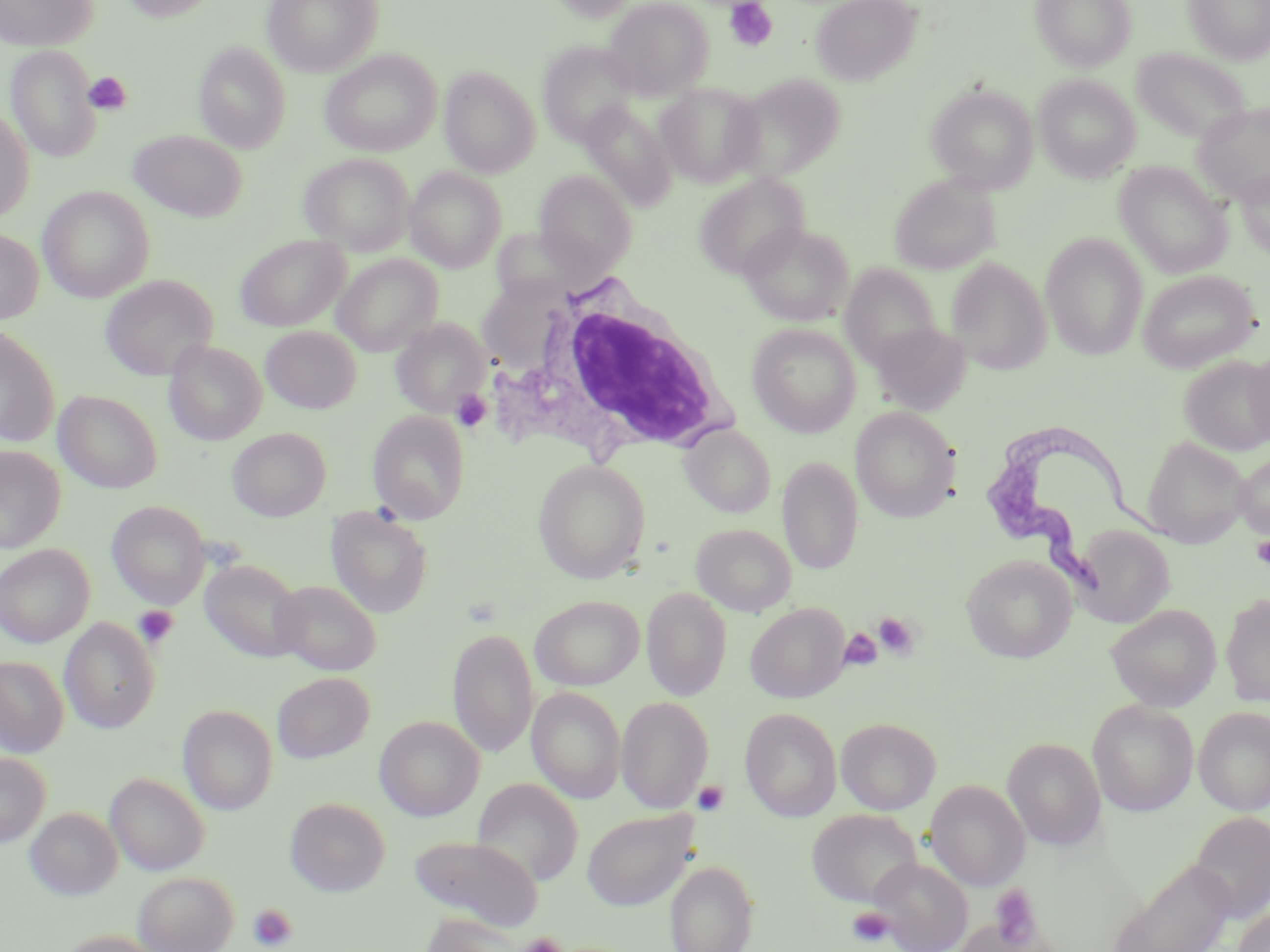

slide-level diagnosis = Trypanosoma brucei
stain = May-Grünwald-Giemsa
field of view = single
modality = light microscopy
uninfected red blood cell locations = approximate bounding boxes as [x1, y1, x2, y2] in pixels: [0, 0, 99, 51], [120, 0, 221, 22], [263, 0, 384, 76], [550, 0, 642, 22], [603, 0, 714, 99], [811, 0, 921, 86], [1031, 0, 1137, 71], [1184, 0, 1270, 64], [194, 42, 291, 153], [537, 42, 643, 147], [4, 44, 101, 162], [1131, 47, 1252, 145], [320, 50, 441, 157], [439, 66, 540, 177], [728, 72, 846, 182], [1035, 75, 1140, 181], [656, 82, 765, 187], [926, 82, 1039, 193], [579, 101, 677, 211], [1193, 101, 1270, 206], [0, 107, 34, 222], [128, 130, 246, 222], [300, 153, 415, 255], [1114, 161, 1232, 277], [405, 167, 506, 272], [1234, 167, 1270, 260], [534, 171, 636, 275], [694, 173, 809, 280], [889, 174, 1000, 275], [38, 186, 154, 302], [739, 223, 854, 326], [489, 227, 595, 304], [0, 228, 43, 325], [1040, 233, 1148, 360], [236, 234, 350, 332], [333, 254, 444, 356], [946, 257, 1051, 375], [840, 263, 942, 369], [1138, 270, 1260, 372], [100, 275, 218, 381], [391, 318, 491, 417], [869, 322, 972, 416], [0, 323, 59, 447], [747, 323, 861, 437], [261, 326, 361, 413], [164, 340, 266, 445], [1246, 347, 1270, 449], [1180, 356, 1270, 456], [54, 390, 163, 494], [850, 407, 960, 522], [369, 410, 469, 524], [680, 423, 775, 517], [227, 427, 331, 521], [1142, 436, 1251, 547], [0, 445, 66, 553], [1233, 451, 1270, 541], [778, 455, 863, 575], [533, 459, 650, 582], [107, 501, 209, 608], [326, 505, 434, 618], [691, 523, 797, 616], [1071, 524, 1175, 628], [0, 544, 95, 647], [960, 554, 1077, 662], [199, 558, 305, 662], [272, 579, 382, 676], [642, 586, 732, 701], [1220, 593, 1270, 707], [530, 595, 644, 690], [746, 603, 849, 703], [1105, 604, 1221, 711], [59, 617, 159, 733], [448, 628, 538, 758], [0, 656, 69, 757], [272, 671, 375, 763], [527, 687, 626, 804], [616, 696, 714, 814], [1087, 699, 1199, 816], [177, 704, 278, 814], [1194, 706, 1270, 815], [739, 707, 842, 821], [374, 716, 484, 821], [836, 717, 940, 815], [1003, 737, 1106, 851], [0, 752, 51, 848], [105, 772, 209, 876], [472, 778, 583, 886], [925, 780, 1030, 891], [285, 797, 390, 897], [25, 806, 123, 900], [582, 808, 698, 911], [807, 809, 923, 908], [1189, 810, 1270, 924], [409, 835, 543, 931], [868, 857, 973, 952], [1109, 859, 1237, 952], [665, 860, 758, 952], [133, 871, 238, 952], [1233, 908, 1270, 952], [419, 917, 524, 952], [953, 918, 1039, 952], [51, 930, 169, 952]
preparation = thin blood smear
Trypanosoma brucei locations = approximate bounding boxes as [x1, y1, x2, y2] in pixels: [979, 419, 1186, 599]
image size = 1270×952 pixels
magnification = 1000x
platelet locations = approximate bounding boxes as [x1, y1, x2, y2] in pixels: [725, 1, 777, 52], [84, 72, 131, 115], [451, 389, 492, 433], [1252, 536, 1270, 569], [133, 605, 179, 648], [873, 611, 921, 660], [839, 628, 882, 671], [692, 779, 730, 817], [989, 884, 1041, 947], [248, 903, 298, 951], [848, 906, 896, 947], [517, 933, 566, 952]
white blood cell locations = approximate bounding boxes as [x1, y1, x2, y2] in pixels: [488, 282, 735, 469]